Give the extent of all uninfected red blood cells.
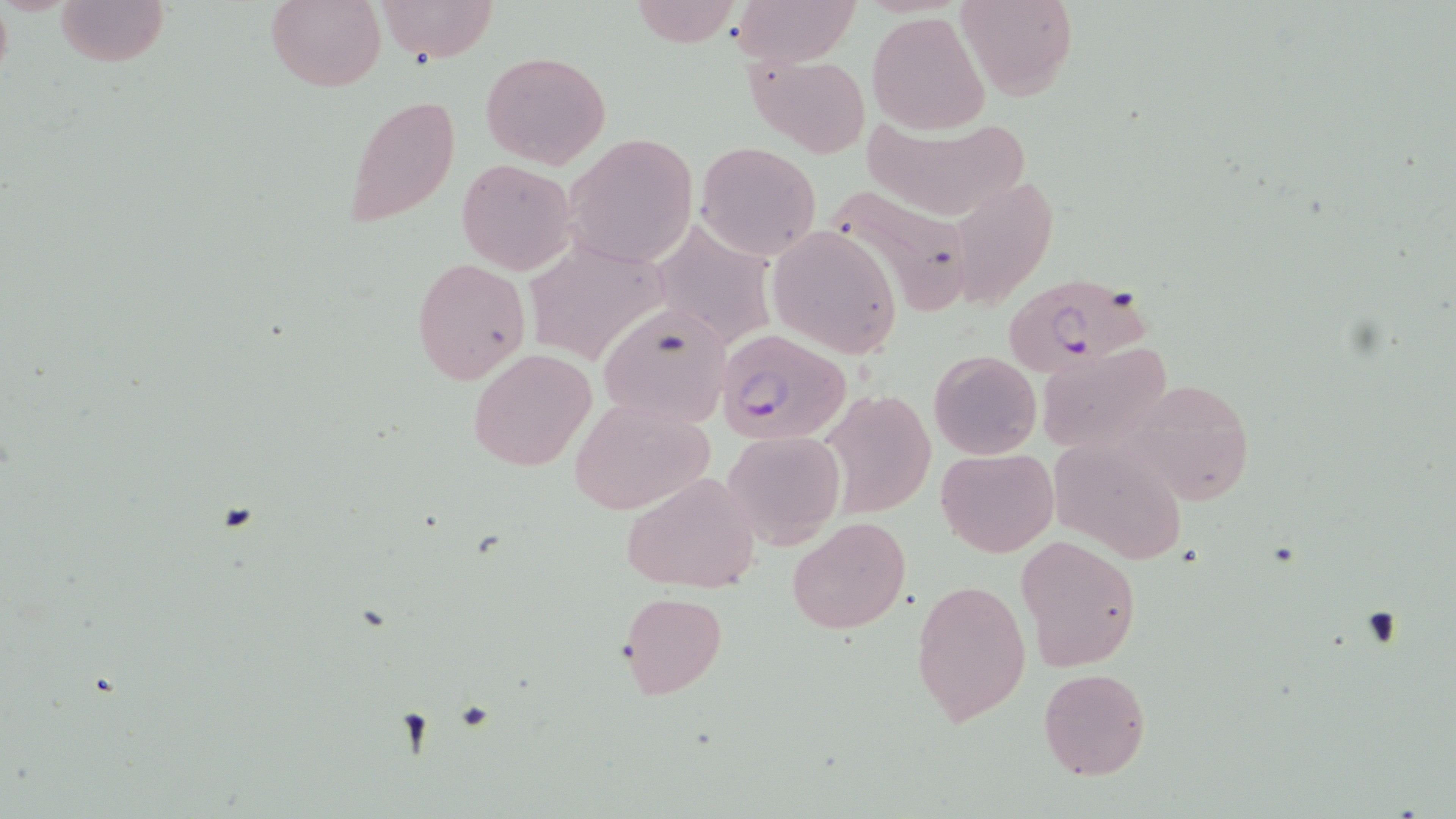

Approximate bounding boxes as (x1,y1)-(x2,y2) corner pairs in pixels.
Uninfected red blood cells: (56,0)-(169,68), (263,0)-(387,91), (374,0)-(498,62), (629,0)-(741,46), (731,0)-(861,67), (954,0)-(1078,100), (868,11)-(990,134), (481,51)-(612,169), (747,51)-(871,158), (344,94)-(461,231), (861,118)-(1032,221), (565,134)-(699,268), (695,142)-(822,260), (456,158)-(578,274), (826,181)-(972,314), (949,183)-(1067,319), (653,210)-(782,351), (771,226)-(898,358), (521,236)-(676,367), (410,258)-(530,386), (596,303)-(733,431), (1036,342)-(1173,455), (467,348)-(596,472), (929,351)-(1042,459), (1130,376)-(1255,505), (823,390)-(935,518), (570,395)-(716,515), (722,430)-(843,548), (1048,437)-(1189,568), (936,448)-(1057,557), (620,471)-(761,594), (787,516)-(910,635), (1015,535)-(1142,672), (911,579)-(1032,728), (618,590)-(729,699), (1038,667)-(1151,781).

slide-level diagnosis = Plasmodium falciparum
modality = optical microscopy
field of view = single
preparation = thin blood film
magnification = 1000x
image size = 1456×819 pixels
stain = May-Grünwald-Giemsa
Plasmodium falciparum-infected red blood cell locations = approximate bounding boxes as (x1,y1)-(x2,y2) corner pairs in pixels: (1003,273)-(1151,374), (715,329)-(852,446)